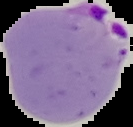
preparation = thin blood film
malaria status = parasitized
image size = 133×127 pixels
image type = segmented cell region with the area outside set to black